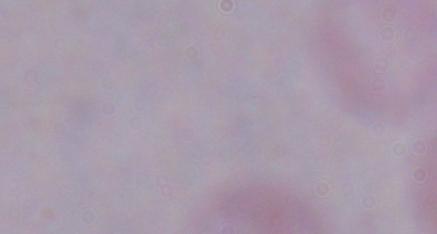

Summary:
  - Magnification: 1000x
  - Modality: photomicrograph
  - Identification: trypanosome